Report the malaria status of this cell.
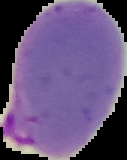

It is parasitized.

image type = segmented cell region with the area outside set to black
preparation = thin blood smear
image size = 127×160 pixels